Identify the parasite.
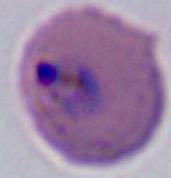
Plasmodium.

Summary:
  - Magnification: 400x or 1000x
  - Modality: photomicrograph